Report the malaria status of this cell.
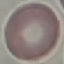

It is uninfected.

capture = smartphone through the microscope eyepiece
preparation = thin smear
image type = cell patch, automatically extracted from a larger field of view and resized to 64 × 64 pixels
stain = Giemsa